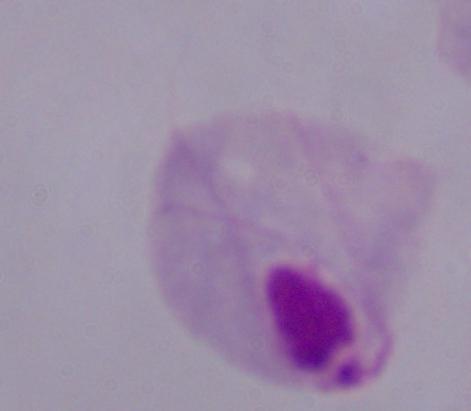
magnification = 1000x
identification = trichomonad
modality = photomicrograph